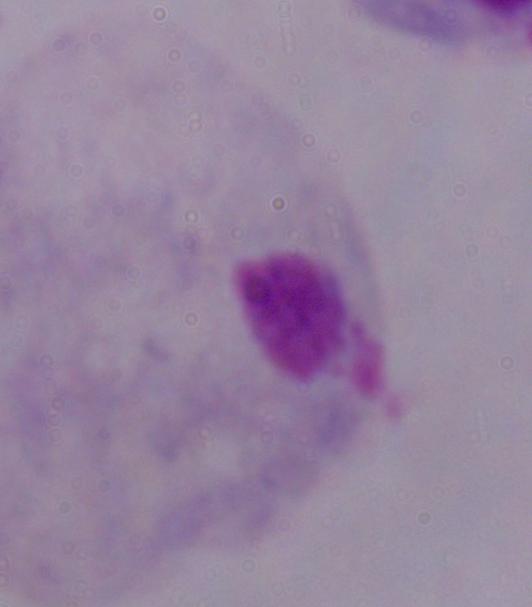
modality = micrograph
magnification = 1000x
identification = trichomonad